Locate every blood parasite and identify its species.
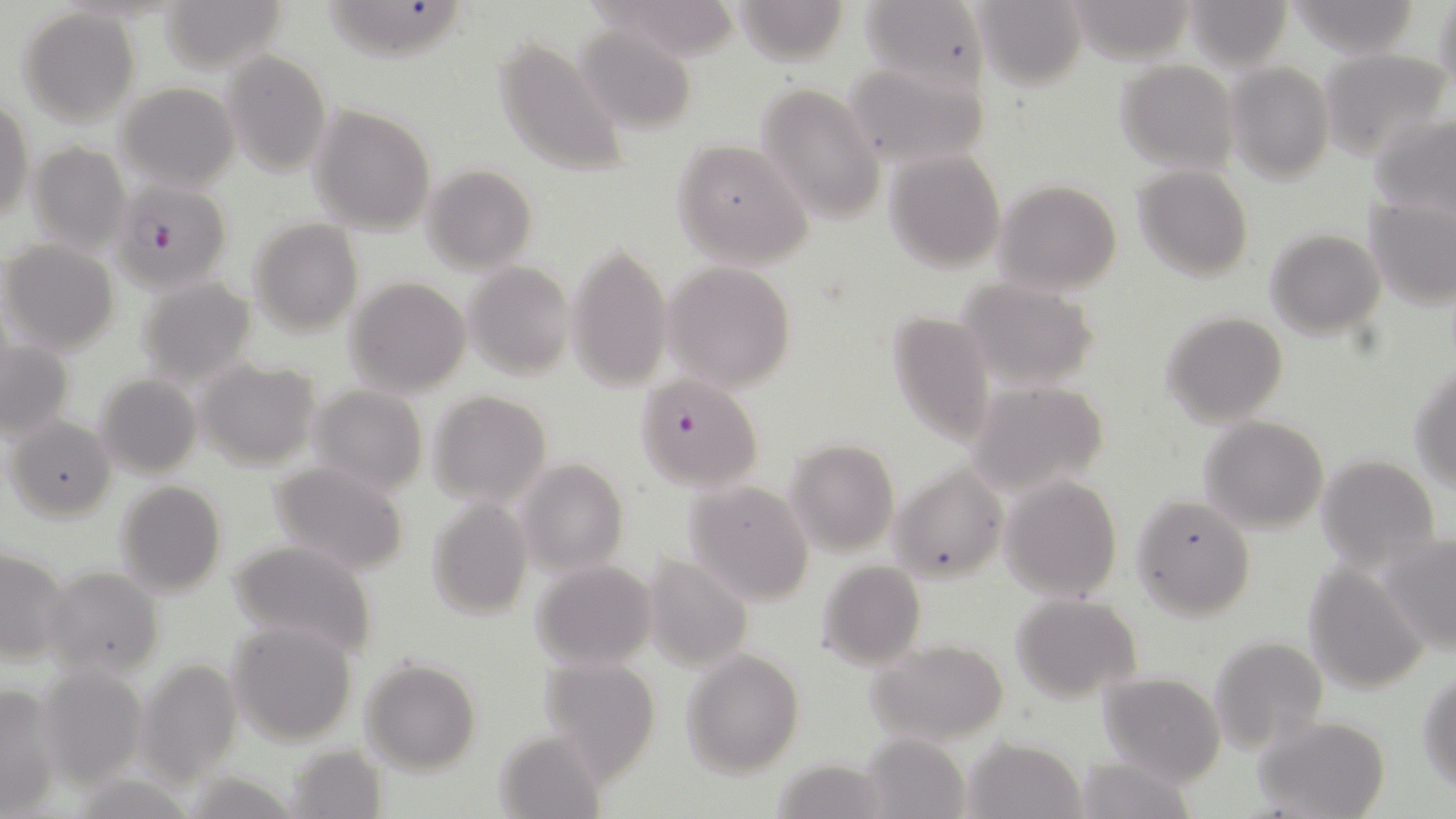
Approximate bounding boxes as (x1, y1, x2, y2) in pixels.
Plasmodium falciparum-infected red blood cells: (109, 176, 234, 317), (634, 373, 764, 493).
No Plasmodium ovale, Plasmodium malariae, Plasmodium vivax, Babesia divergens, or Trypanosoma brucei observed.

Uninfected red blood cell locations: (732, 0, 852, 66), (859, 0, 989, 91), (974, 0, 1087, 90), (1184, 0, 1294, 70), (1288, 0, 1423, 58), (1433, 0, 1456, 93), (157, 1, 288, 74), (324, 2, 464, 60), (586, 5, 741, 56), (19, 7, 140, 127), (573, 28, 698, 134), (492, 32, 631, 177), (1318, 46, 1453, 159), (222, 50, 333, 176), (842, 58, 990, 170), (1114, 58, 1239, 173), (1227, 62, 1335, 183), (114, 82, 240, 193), (756, 82, 885, 228), (0, 100, 32, 223), (309, 102, 436, 234), (1369, 111, 1456, 219), (672, 139, 814, 270), (26, 143, 132, 256), (882, 149, 1007, 273), (422, 164, 538, 273), (1132, 166, 1254, 281), (993, 180, 1122, 297), (1363, 193, 1456, 308), (249, 218, 362, 339), (1265, 228, 1385, 340), (1, 239, 119, 355), (563, 239, 675, 394), (663, 261, 798, 391), (464, 262, 575, 380), (134, 275, 258, 385), (345, 276, 473, 397), (959, 277, 1100, 390), (886, 311, 994, 447), (1160, 311, 1289, 427), (0, 333, 76, 446), (195, 359, 322, 469), (1410, 364, 1456, 491), (94, 373, 202, 479), (966, 380, 1108, 498), (308, 384, 429, 497), (428, 390, 552, 507), (4, 414, 115, 521), (1198, 417, 1329, 534), (785, 437, 899, 557), (1316, 454, 1442, 570), (518, 457, 628, 576), (265, 460, 412, 577), (889, 463, 1009, 583), (1001, 475, 1121, 602), (685, 480, 816, 604), (114, 481, 226, 600), (1131, 494, 1257, 621), (426, 499, 534, 621), (1379, 535, 1456, 656), (225, 539, 380, 662), (1, 546, 70, 667), (643, 555, 753, 672), (815, 559, 926, 671), (530, 560, 658, 671), (1303, 561, 1430, 694), (43, 565, 164, 680), (1012, 594, 1143, 703), (227, 620, 359, 747), (1209, 635, 1328, 754), (867, 639, 1009, 746), (681, 649, 804, 777), (537, 655, 661, 779), (135, 657, 244, 786), (361, 658, 481, 774), (37, 664, 149, 789), (1418, 668, 1456, 792), (1098, 672, 1226, 787), (0, 682, 62, 818), (1255, 717, 1391, 819), (494, 731, 608, 818), (859, 732, 970, 819), (964, 736, 1087, 818), (287, 743, 390, 818), (1073, 755, 1198, 818), (769, 758, 889, 817). Slide-level diagnosis: Plasmodium falciparum. Optical microscopy. 1000x magnification. May-Grünwald-Giemsa stain. Image is 1456×819 pixels. Thin blood film. One field of a larger specimen.